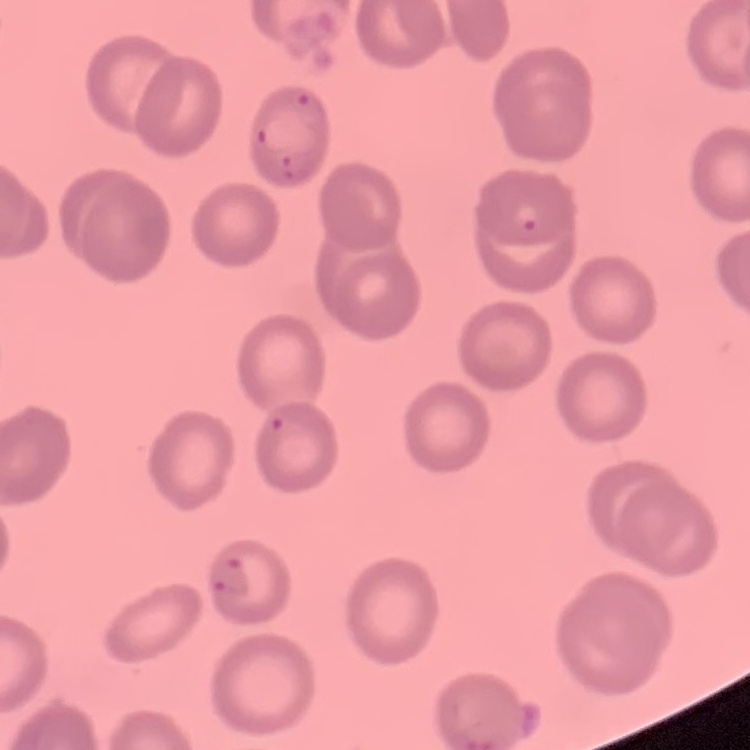

Summary:
  - Erythrocyte morphology: no rouleaux formation
  - Preparation: thin peripheral smear
  - Stain: Field's or Giemsa
  - Image type: one tile cut from a larger photomicrograph